Assess this cell for malaria.
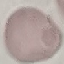

It is uninfected.

Giemsa-stained preparation. Thin smear of blood. Automatically extracted cell patch, resized to 64 × 64 pixels. Photographed with a smartphone camera at the microscope eyepiece.